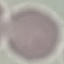 Result: no malaria parasites seen. Thin smear of blood. Automatically extracted cell patch, resized to 64 × 64 pixels. Photographed with a smartphone camera at the microscope eyepiece. Giemsa stain.